Name the cell type shown.
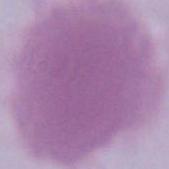
An erythrocyte.

Captured at 1000x magnification. Micrograph.